Report the malaria status of this cell.
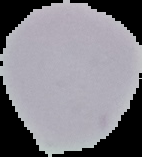

Uninfected.

{
  "preparation": "thin blood smear",
  "image_size": "142×157 pixels",
  "image_type": "segmented cell region on a black background"
}